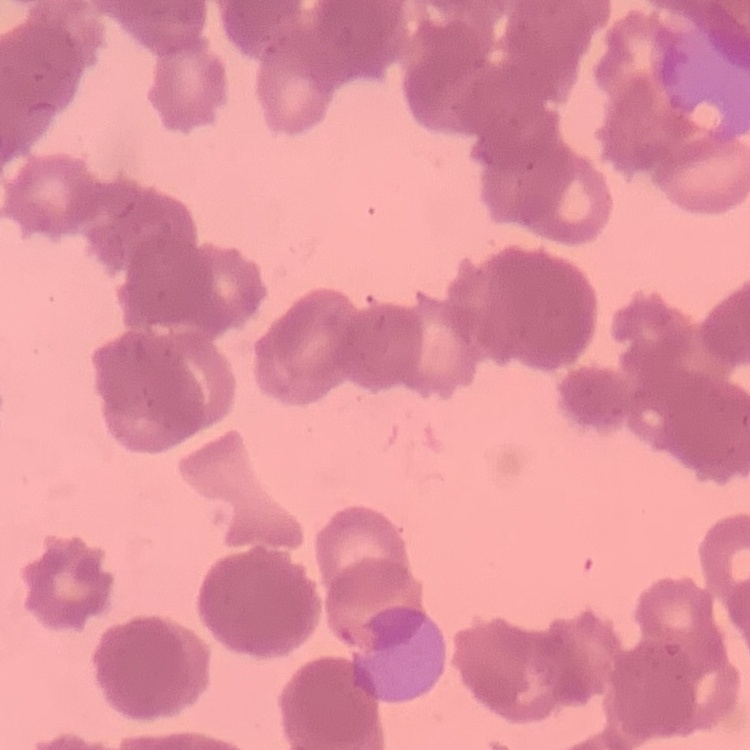 The erythrocytes exhibit rouleaux formation. One tile cut from a larger photomicrograph. Field's or Giemsa stain. Thin blood smear.